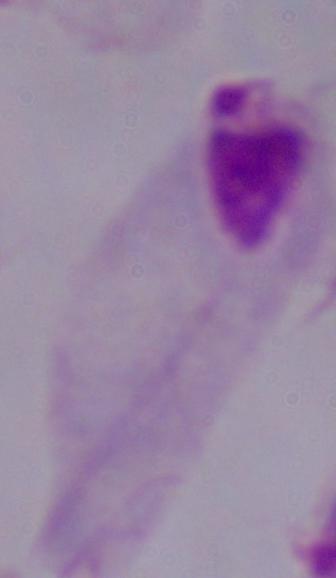
{
  "modality": "micrograph",
  "magnification": "1000x",
  "identification": "trichomonad"
}